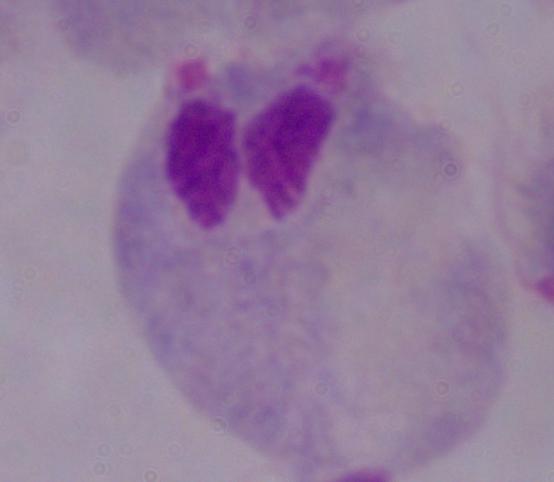 Micrograph. A trichomonad is shown. Captured at 1000x magnification.